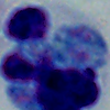

Summary:
  - Identification: leukocyte
  - Modality: micrograph
  - Magnification: 1000x